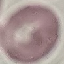
malaria status = uninfected
image type = cell patch, automatically extracted from a larger field of view and resized to 64 × 64 pixels
capture = smartphone camera at the microscope eyepiece
stain = Giemsa
preparation = thin smear